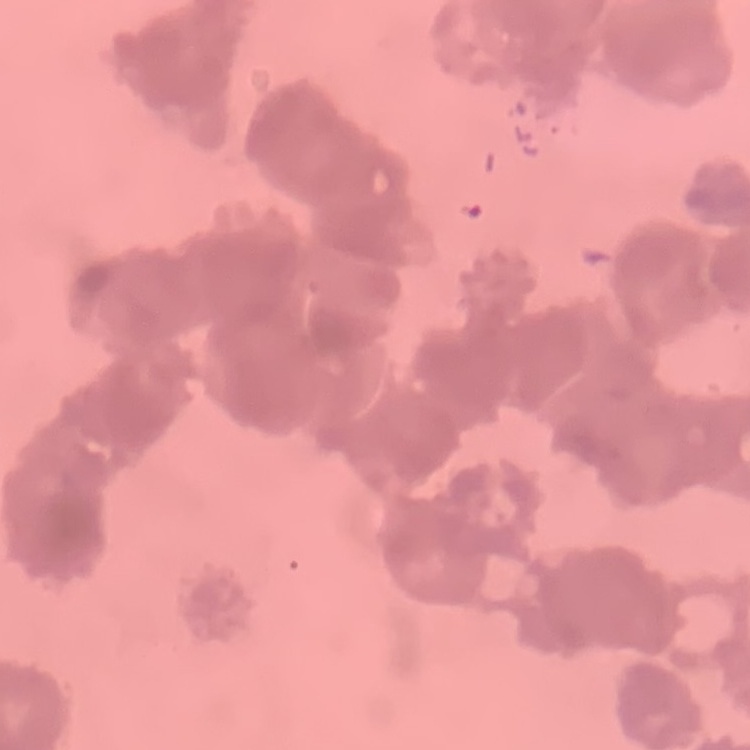
The erythrocytes exhibit rouleaux formation. Stained with either Field's or Giemsa. Thin blood film. One tile cut from a larger photomicrograph.